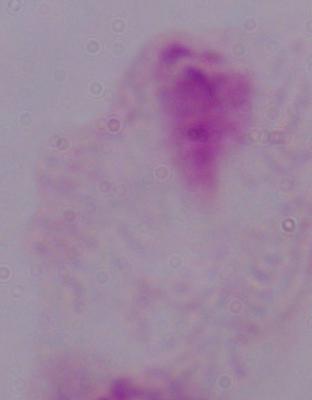

magnification: 1000x
identification: trichomonad
modality: photomicrograph